Describe the morphology of the erythrocytes.
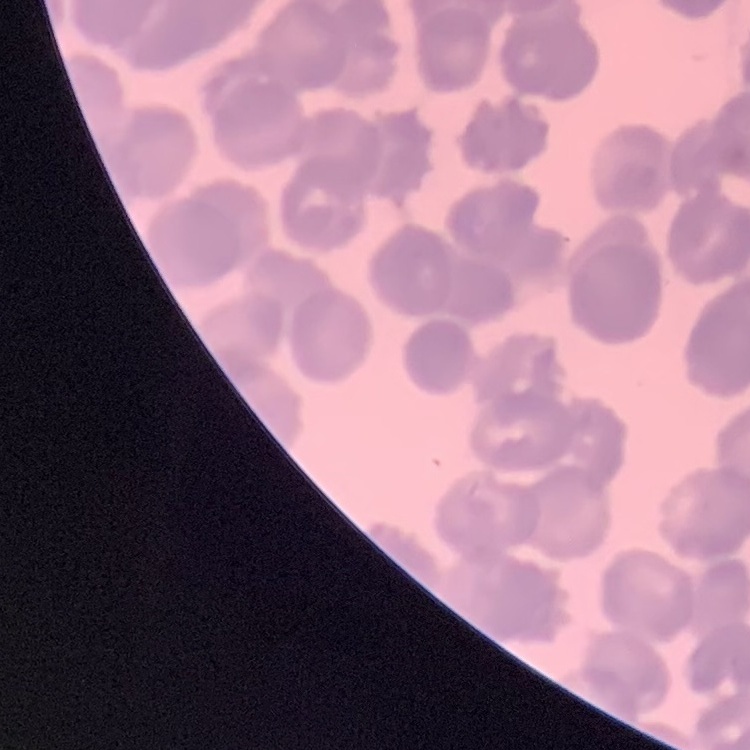

They show rouleaux formation.

Summary:
  - Image type: one tile cut from a larger photomicrograph
  - Preparation: thin blood smear
  - Stain: Field's or Giemsa